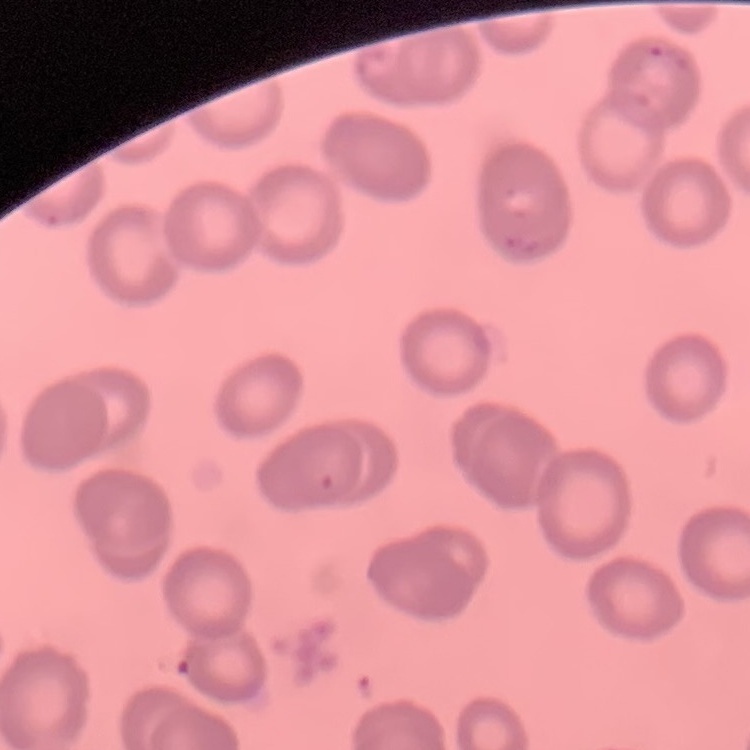
Summary:
  - Red blood cell morphology: no rouleaux formation
  - Stain: Field's or Giemsa
  - Image type: one tile cut from a larger photomicrograph
  - Preparation: thin peripheral smear